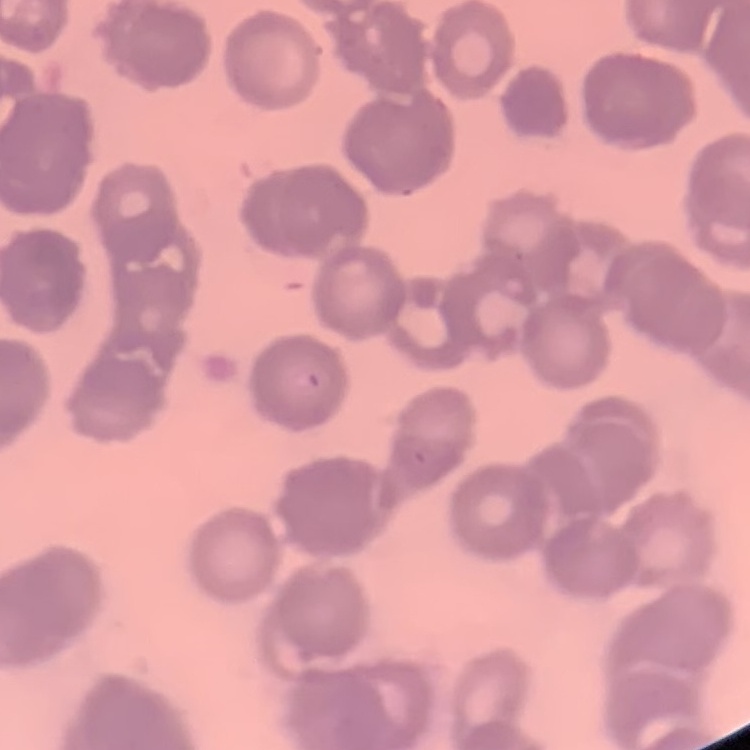

Summary:
  - Red blood cell morphology: rouleaux formation
  - Preparation: thin peripheral smear
  - Stain: Field's or Giemsa
  - Image type: one tile cut from a larger photomicrograph